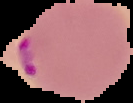

Summary:
  - Image size: 133×103 pixels
  - Preparation: thin blood smear
  - Image type: segmented cell region with the area outside set to black
  - Malaria status: parasitized